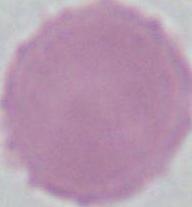
Summary:
  - Modality: photomicrograph
  - Magnification: 1000x
  - Identification: red blood cell